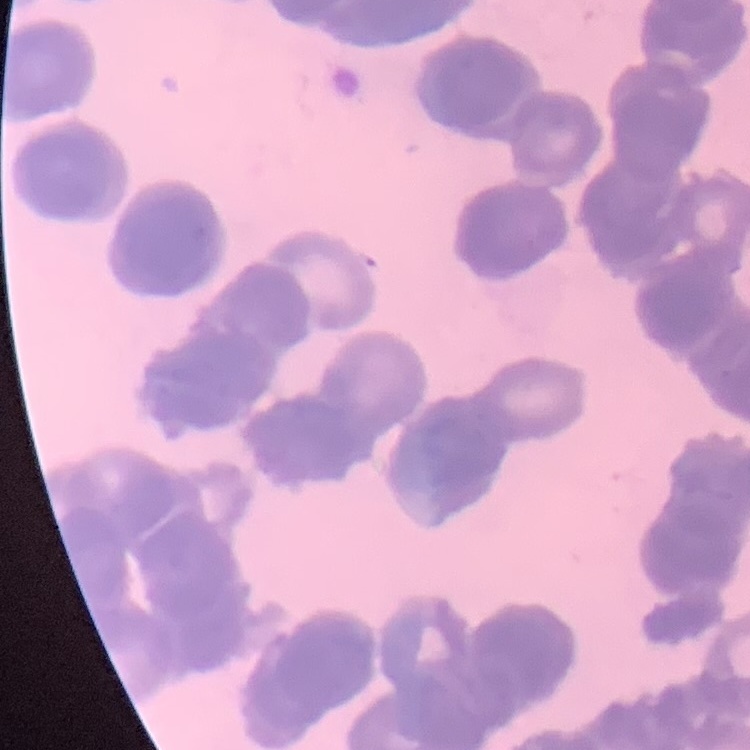

red blood cell morphology = rouleaux formation
stain = Field's or Giemsa
preparation = thin blood film
image type = square crop of a larger photomicrograph